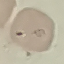
Summary:
  - Malaria status: uninfected
  - Preparation: thin blood film
  - Image type: automatically extracted cell patch, resized to 64 × 64 pixels
  - Stain: Giemsa
  - Capture: smartphone through the microscope eyepiece